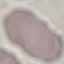
result: negative for malaria parasites
image_type: automatically extracted cell patch, resized to 64 × 64 pixels
stain: Giemsa
preparation: thin blood film
capture: smartphone through the microscope eyepiece